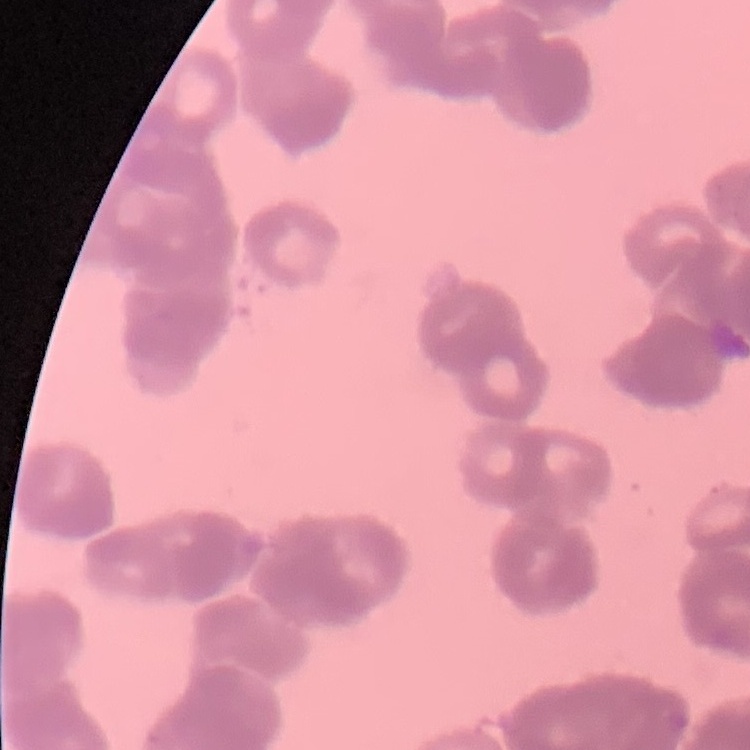
Summary:
  - Erythrocyte morphology: rouleaux formation
  - Preparation: thin blood smear
  - Stain: Field's or Giemsa
  - Image type: one tile cut from a larger photomicrograph